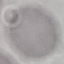
malaria status = uninfected
capture = smartphone camera at the microscope eyepiece
preparation = thin smear
image type = cell patch, automatically extracted from a larger field of view and resized to 64 × 64 pixels
stain = Giemsa